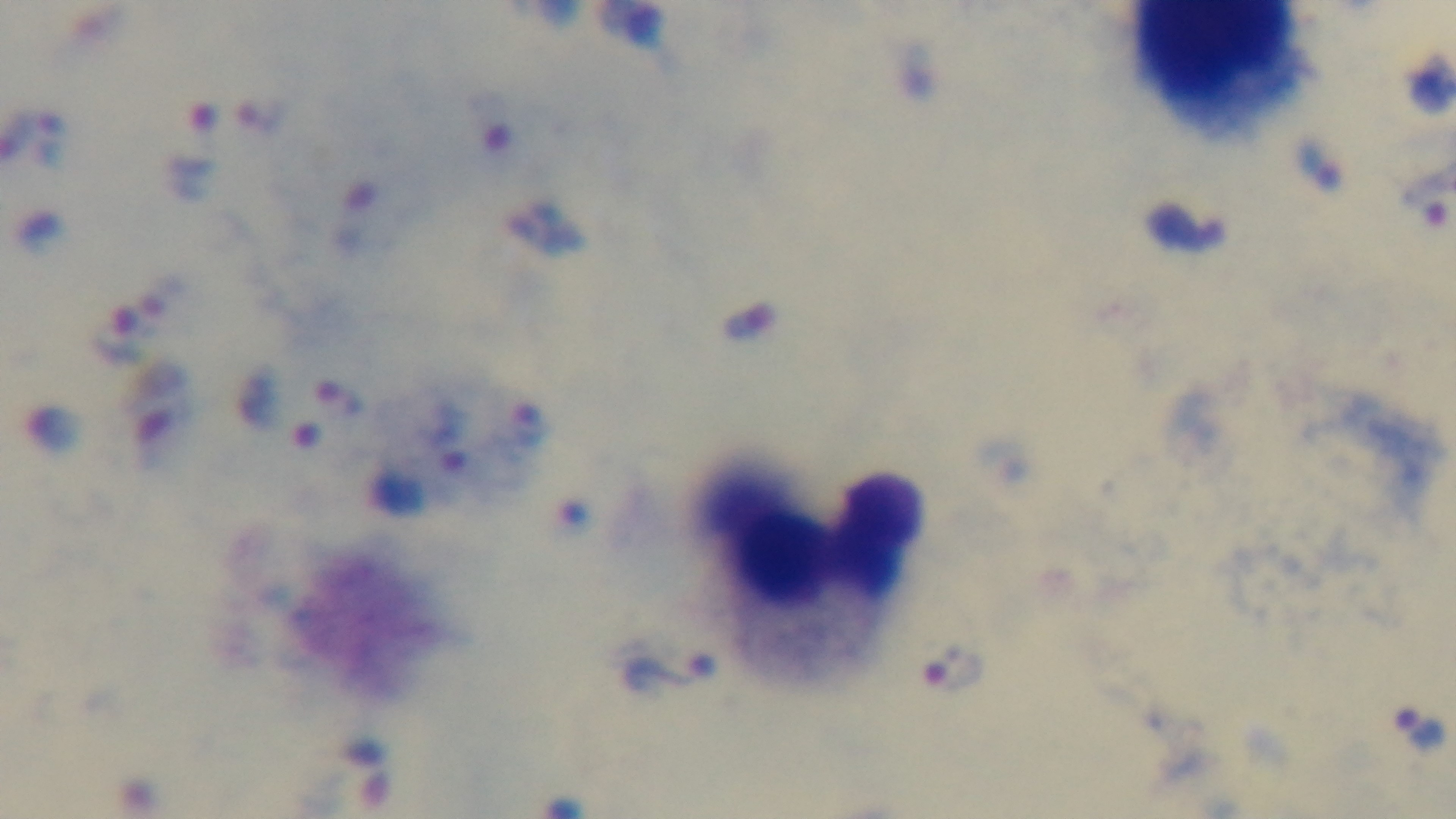

{
  "objective": "100x oil immersion",
  "field_of_view": "single",
  "malaria_status": "positive",
  "preparation": "thick",
  "capture": "mounted 4K digital camera",
  "modality": "light microscopy",
  "stain": "Giemsa"
}